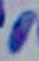
Summary:
  - Identification: Toxoplasma gondii
  - Modality: photomicrograph
  - Magnification: 1000x